Locate every blood parasite and identify its species.
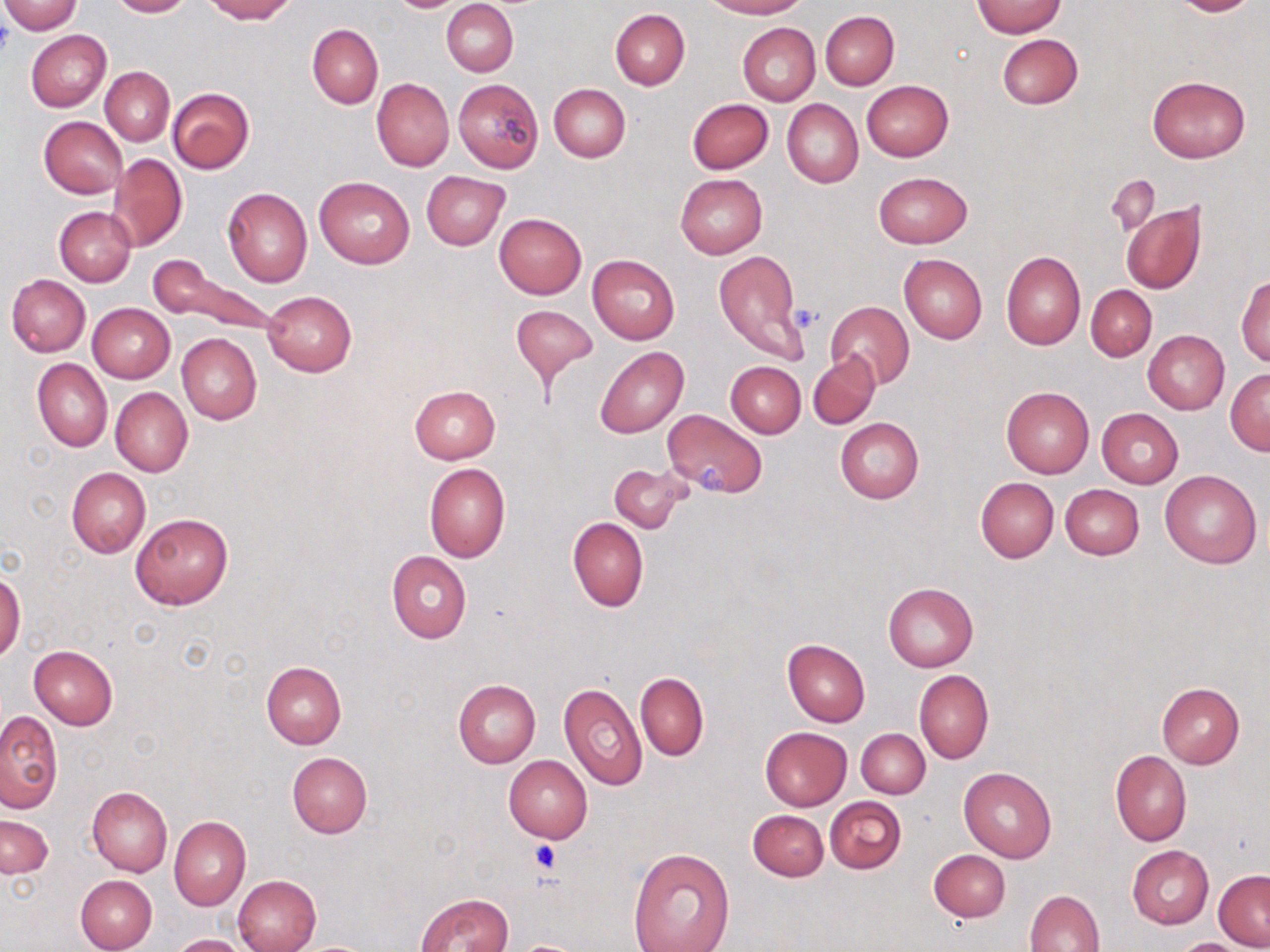
No blood parasites seen.

Approximate bounding boxes as (x1, y1, x2, y2) in pixels. Uninfected red blood cell locations: (0, 0, 84, 34), (107, 0, 193, 17), (202, 0, 296, 22), (702, 0, 807, 18), (1169, 0, 1258, 16), (442, 1, 518, 76), (973, 1, 1065, 38), (610, 8, 690, 90), (821, 11, 898, 89), (737, 22, 821, 104), (306, 24, 383, 110), (25, 29, 111, 112), (996, 33, 1083, 109), (101, 67, 174, 144), (1146, 75, 1251, 163), (453, 77, 544, 173), (372, 79, 454, 170), (862, 81, 954, 162), (549, 84, 631, 162), (168, 87, 255, 173), (687, 99, 774, 174), (782, 100, 863, 189), (39, 117, 126, 199), (108, 153, 187, 252), (422, 171, 509, 250), (873, 171, 972, 248), (675, 173, 767, 258), (1106, 174, 1159, 237), (314, 176, 414, 268), (221, 187, 313, 286), (1121, 201, 1207, 295), (54, 207, 136, 287), (494, 213, 586, 300), (714, 250, 807, 363), (1002, 251, 1085, 350), (898, 252, 987, 343), (587, 254, 680, 344), (152, 258, 283, 339), (7, 274, 91, 356), (1236, 275, 1270, 367), (1086, 284, 1156, 361), (263, 291, 356, 376), (825, 302, 915, 389), (87, 303, 175, 383), (511, 305, 599, 385), (1143, 330, 1229, 414), (177, 333, 262, 424), (596, 346, 688, 438), (807, 352, 881, 429), (33, 358, 112, 451), (726, 361, 806, 438), (1225, 370, 1270, 455), (409, 384, 500, 463), (1001, 386, 1094, 478), (110, 388, 192, 476), (663, 409, 768, 498), (1097, 409, 1183, 487), (834, 418, 923, 504), (607, 461, 692, 534), (424, 463, 510, 562), (66, 467, 150, 557), (1160, 469, 1262, 569), (975, 478, 1059, 562), (1061, 483, 1144, 560), (130, 512, 234, 609), (568, 518, 649, 611), (386, 551, 472, 643), (1, 570, 26, 662), (883, 582, 978, 672), (782, 639, 870, 726), (28, 645, 118, 729), (261, 661, 347, 748), (914, 669, 993, 764), (636, 672, 708, 761), (453, 680, 541, 768), (559, 680, 647, 789), (1156, 683, 1245, 768), (0, 711, 63, 815), (760, 726, 852, 811), (856, 729, 930, 798), (1110, 750, 1192, 845), (287, 752, 372, 837), (503, 754, 593, 843), (959, 766, 1057, 862), (88, 785, 172, 876), (824, 797, 907, 874), (748, 810, 829, 881), (1, 815, 52, 878), (169, 815, 250, 910), (1127, 845, 1214, 928), (627, 846, 734, 951), (929, 849, 1010, 922), (1214, 870, 1270, 950), (74, 874, 157, 952), (233, 875, 321, 952), (1026, 889, 1105, 952), (417, 893, 514, 952), (170, 933, 248, 952), (1170, 938, 1254, 952), (514, 941, 584, 952). Platelet locations: (788, 304, 821, 334), (696, 462, 731, 494), (531, 840, 560, 873). Slide-level diagnosis: negative for blood parasites. Light microscopy. Thin blood smear. May-Grünwald-Giemsa-stained preparation. One field of a larger specimen. 1000x magnification. Image is 1270×952 pixels.